Classify this cell by malaria status.
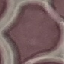
Uninfected.

Summary:
  - Image type: cell patch, automatically extracted from a larger field of view and resized to 64 × 64 pixels
  - Stain: Giemsa
  - Preparation: thin blood smear
  - Capture: smartphone camera at the microscope eyepiece